Classify this cell by malaria status.
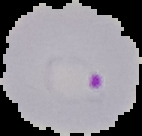
It is parasitized.

Summary:
  - Preparation: thin blood smear
  - Image type: segmented cell region with the area outside set to black
  - Image size: 142×136 pixels